Assess this cell for malaria.
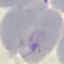

Uninfected.

Automatically extracted cell patch, resized to 64 × 64 pixels. Photographed with a smartphone camera at the microscope eyepiece. Thin smear of blood. Giemsa stain.